Locate platelets.
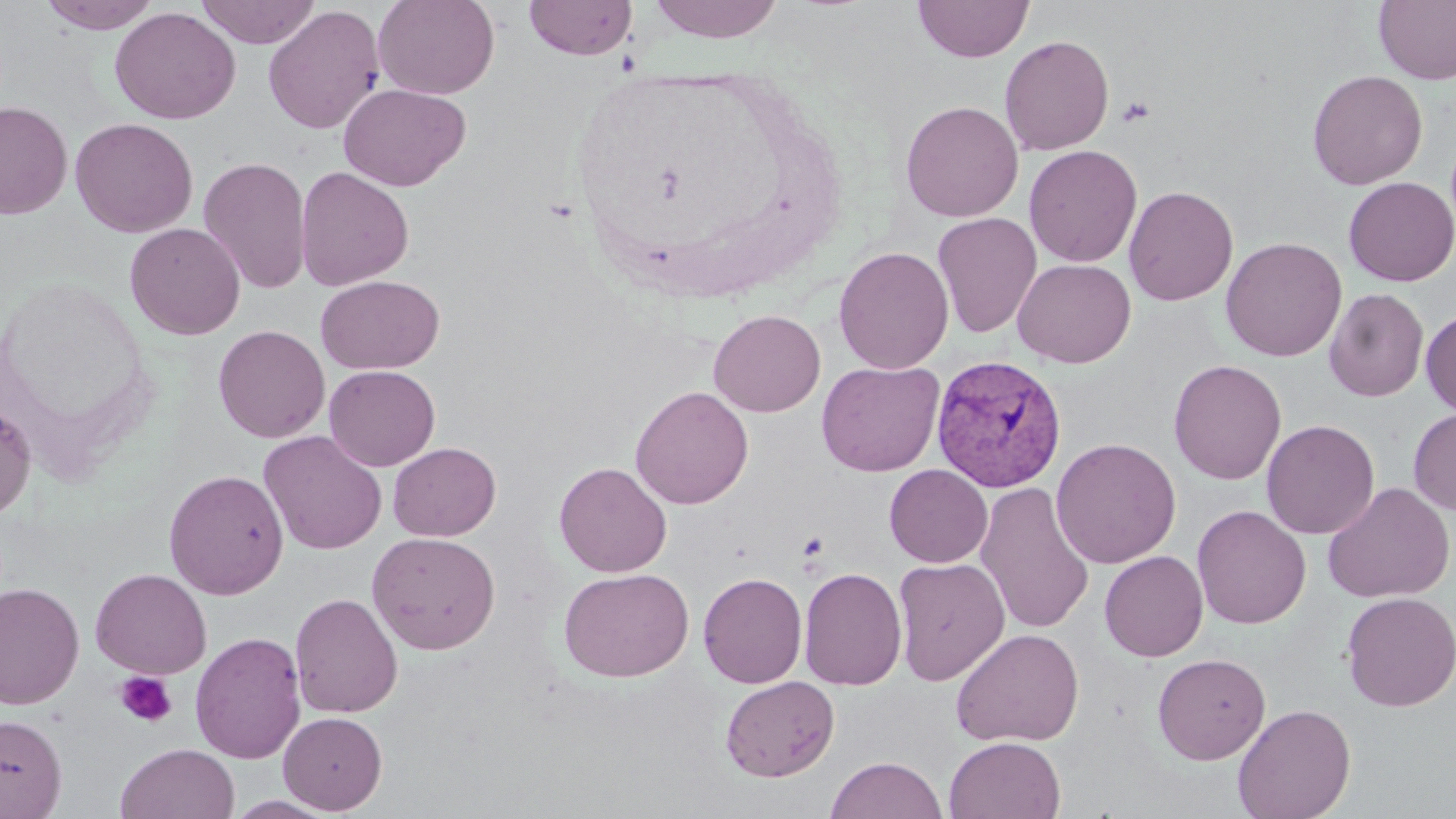
Approximate bounding boxes as [x1, y1, x2, y2] in pixels.
Platelets: [1117, 96, 1155, 128], [798, 531, 829, 563], [114, 671, 178, 727].

Plasmodium vivax-infected red blood cell locations: [931, 354, 1067, 492]. Uninfected red blood cell locations: [39, 0, 162, 33], [195, 0, 322, 48], [373, 0, 499, 99], [524, 0, 637, 60], [648, 0, 785, 43], [913, 0, 1034, 62], [1373, 0, 1456, 85], [263, 4, 385, 135], [109, 6, 241, 125], [999, 34, 1114, 156], [1307, 69, 1428, 190], [337, 82, 471, 191], [0, 100, 73, 219], [900, 100, 1023, 222], [70, 117, 198, 237], [1024, 144, 1142, 267], [198, 156, 312, 294], [295, 166, 414, 290], [1343, 177, 1456, 286], [1123, 185, 1238, 306], [932, 212, 1042, 339], [124, 222, 245, 340], [1221, 237, 1347, 362], [833, 245, 954, 374], [1012, 257, 1136, 368], [315, 274, 444, 374], [1324, 288, 1428, 402], [708, 309, 826, 417], [1421, 310, 1456, 417], [213, 324, 330, 443], [1168, 359, 1287, 485], [816, 360, 945, 477], [324, 365, 440, 471], [630, 386, 753, 509], [0, 399, 36, 521], [1408, 408, 1456, 516], [1261, 420, 1379, 539], [258, 430, 387, 555], [1051, 437, 1181, 568], [387, 442, 501, 541], [554, 462, 672, 577], [884, 464, 993, 567], [164, 469, 289, 600], [975, 481, 1095, 635], [1322, 482, 1455, 603], [1192, 505, 1312, 630], [366, 532, 502, 655], [1099, 550, 1208, 661], [893, 557, 1009, 686], [90, 567, 212, 679], [798, 567, 907, 690], [558, 568, 694, 682], [698, 572, 807, 688], [0, 581, 84, 710], [1340, 591, 1455, 712], [290, 592, 403, 718], [950, 628, 1084, 747], [190, 631, 306, 763], [1152, 653, 1271, 765], [720, 675, 840, 782], [1232, 703, 1356, 819], [278, 712, 388, 813], [0, 714, 67, 817], [944, 735, 1066, 819], [116, 743, 239, 819], [825, 756, 947, 818], [226, 795, 338, 818]. Slide-level diagnosis: Plasmodium vivax. Optical microscopy. Thin blood film. May-Grünwald-Giemsa-stained preparation. Single field of view. Captured at 1000x magnification. Image is 1456×819 pixels.